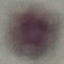

Summary:
  - Malaria status: uninfected
  - Capture: smartphone through the microscope eyepiece
  - Stain: Giemsa
  - Image type: cell patch, automatically extracted from a larger field of view and resized to 64 × 64 pixels
  - Preparation: thin smear